Outline each uninfected red blood cell.
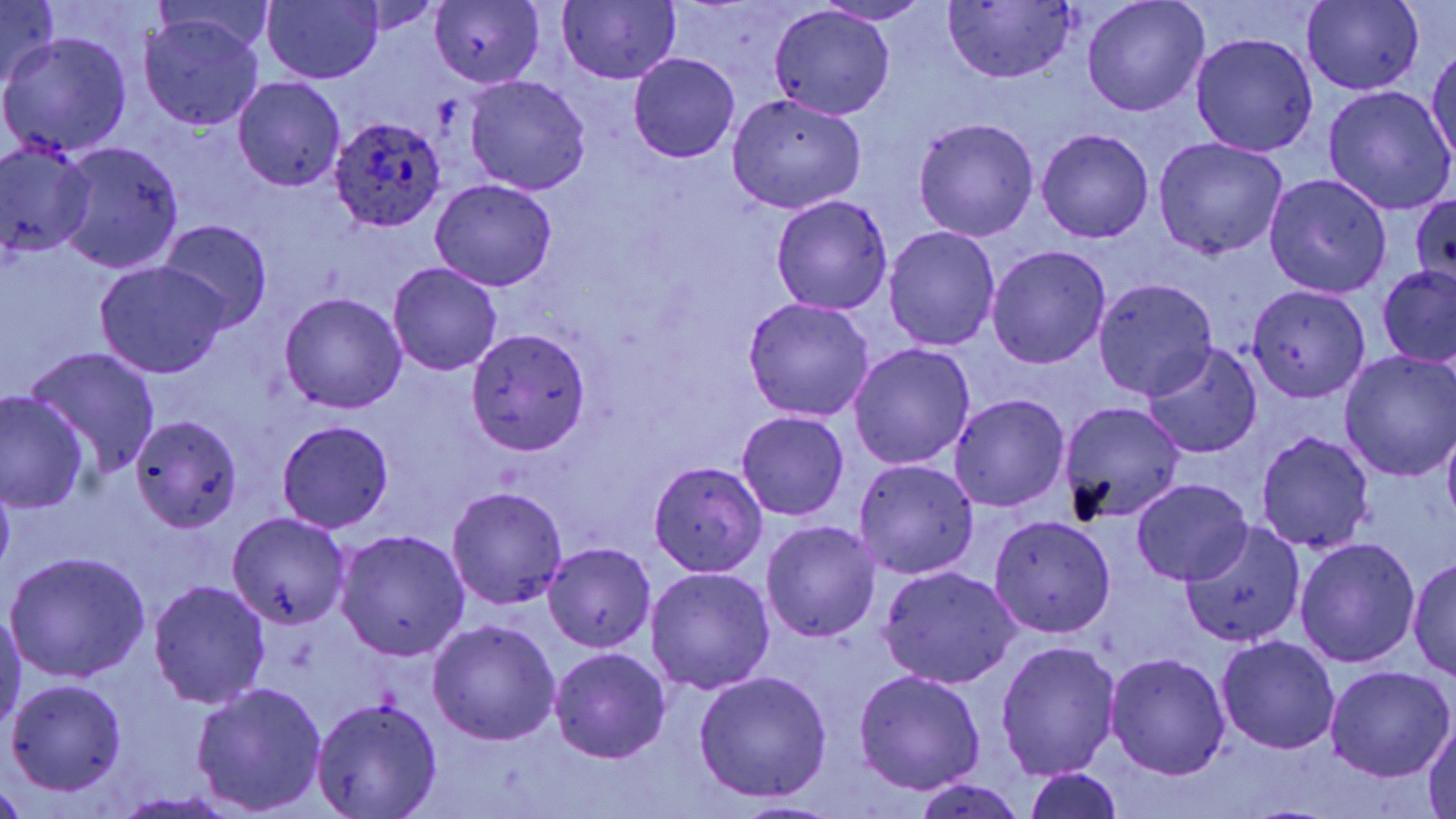

Approximate bounding boxes as [x1, y1, x2, y2] in pixels.
Uninfected red blood cells: [1083, 0, 1209, 118], [0, 1, 60, 93], [261, 1, 383, 85], [430, 1, 545, 87], [558, 1, 680, 85], [816, 1, 935, 24], [341, 2, 444, 35], [942, 2, 1077, 82], [1302, 3, 1425, 95], [769, 5, 896, 121], [139, 12, 263, 131], [2, 31, 133, 155], [1191, 32, 1318, 157], [1427, 44, 1455, 167], [628, 53, 740, 163], [465, 74, 592, 195], [233, 76, 345, 192], [1322, 85, 1455, 215], [726, 93, 867, 214], [914, 118, 1038, 241], [1035, 128, 1154, 244], [1154, 137, 1289, 260], [0, 143, 96, 261], [57, 144, 184, 273], [1264, 173, 1393, 298], [430, 179, 556, 290], [1410, 193, 1456, 287], [771, 196, 894, 315], [157, 219, 273, 330], [883, 226, 1000, 352], [986, 245, 1110, 369], [94, 262, 229, 378], [387, 263, 503, 377], [1378, 265, 1456, 369], [1094, 277, 1220, 400], [1247, 285, 1369, 402], [279, 292, 407, 414], [741, 298, 875, 422], [465, 328, 594, 455], [848, 343, 975, 472], [1143, 343, 1262, 460], [28, 346, 161, 478], [1340, 352, 1456, 482], [1, 391, 89, 513], [949, 393, 1069, 511], [1058, 399, 1186, 525], [736, 410, 851, 521], [130, 415, 242, 533], [279, 421, 394, 533], [1442, 425, 1456, 531], [1253, 430, 1376, 555], [852, 458, 980, 579], [650, 460, 768, 577], [1132, 478, 1252, 584], [0, 480, 13, 576], [446, 485, 568, 609], [226, 512, 351, 628], [990, 515, 1116, 638], [763, 521, 882, 642], [1178, 522, 1305, 650], [336, 530, 470, 662], [1294, 537, 1420, 668], [542, 542, 655, 651], [6, 552, 150, 682], [1409, 556, 1455, 682], [645, 566, 775, 694], [879, 567, 1021, 688], [148, 580, 271, 707], [0, 608, 24, 736], [428, 618, 561, 746], [1216, 635, 1339, 755], [996, 640, 1121, 780], [549, 648, 672, 764], [1105, 652, 1231, 780], [1325, 666, 1453, 781], [852, 670, 986, 794], [694, 672, 834, 802], [7, 678, 128, 795], [192, 682, 327, 816], [310, 696, 443, 818], [1424, 720, 1456, 819], [1023, 767, 1125, 819], [913, 777, 1027, 819], [0, 779, 30, 818], [111, 792, 243, 818], [727, 799, 839, 818].

Plasmodium ovale-infected red blood cell locations: [330, 116, 447, 233]. Slide-level diagnosis: Plasmodium ovale. Thin blood smear. Light microscopy. Single field of view. May-Grünwald-Giemsa-stained preparation. Image is 1456×819 pixels. 1000x magnification.